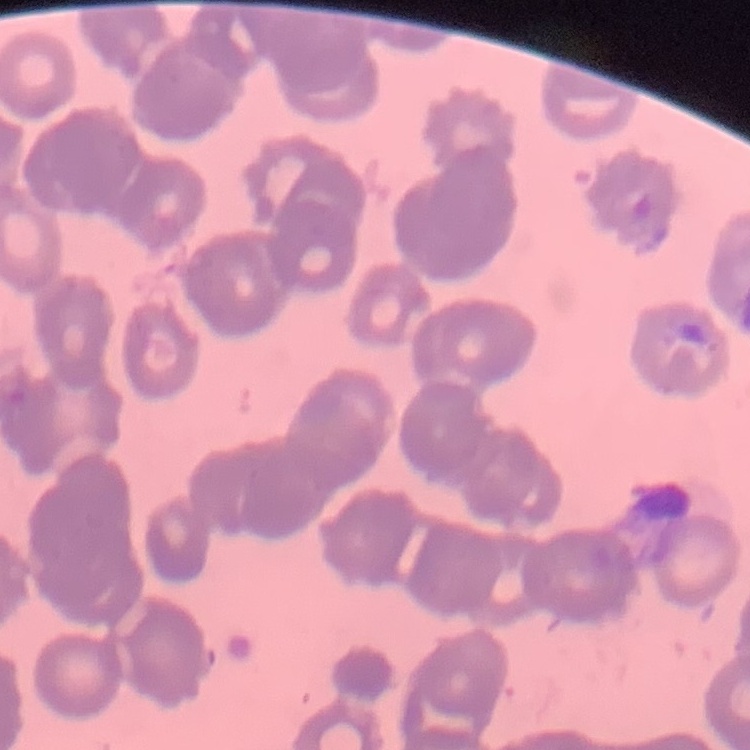
Summary:
  - Erythrocyte morphology: rouleaux formation
  - Stain: Field's or Giemsa
  - Preparation: thin blood smear
  - Image type: square crop of a larger photomicrograph